Identify the parasite.
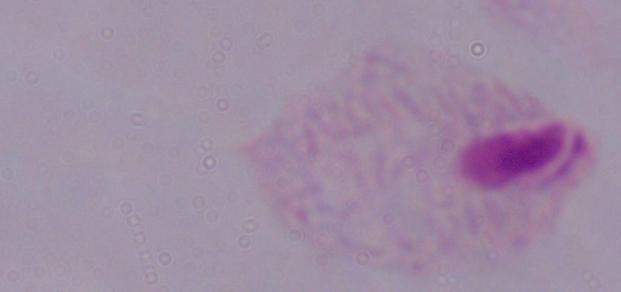
This is a trichomonad.

Summary:
  - Magnification: 1000x
  - Modality: photomicrograph